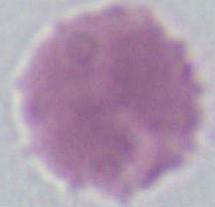

{
  "identification": "red blood cell",
  "modality": "micrograph",
  "magnification": "1000x"
}